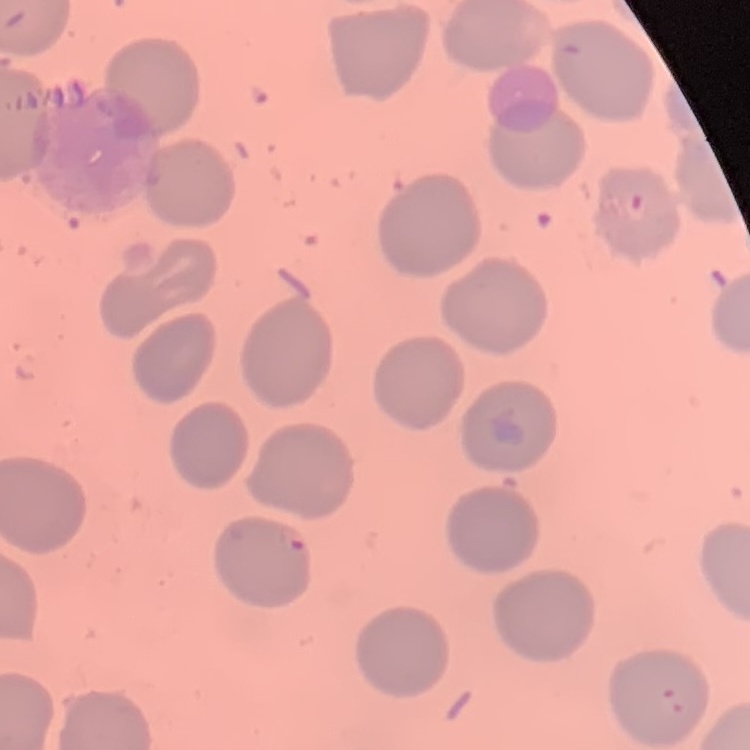

red blood cell morphology = no rouleaux formation
preparation = thin blood film
stain = Field's or Giemsa
image type = one tile cut from a larger photomicrograph